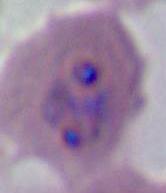

Summary:
  - Magnification: 400x or 1000x
  - Modality: micrograph
  - Identification: Plasmodium